Evaluate for Plasmodium parasites.
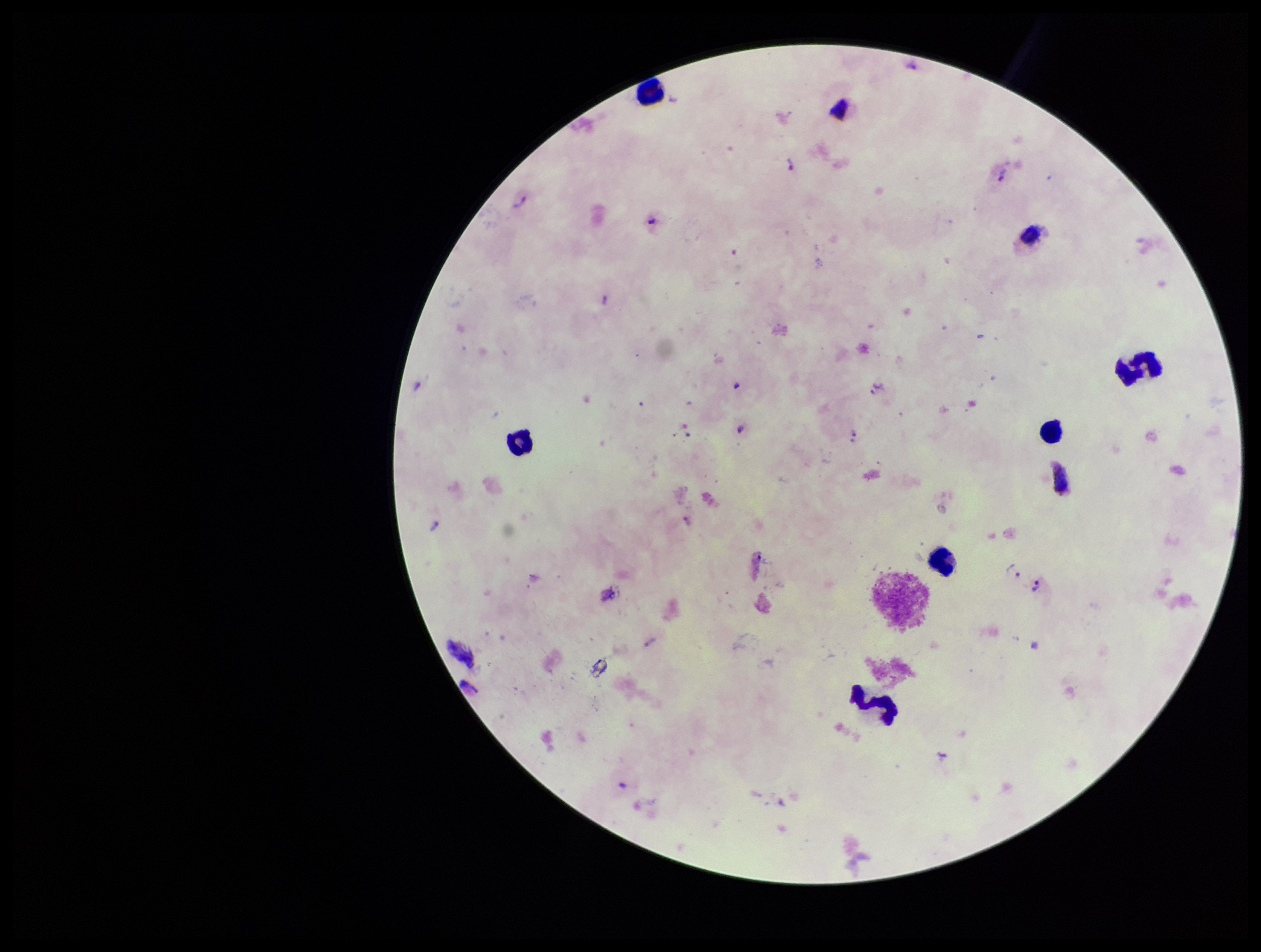
Identified.

stain = Giemsa
parasite count = 11
image size = 1261×952 pixels
patient malaria status = positive
preparation = thick smear
capture = smartphone photograph through the microscope eyepiece
species reported for this patient = Plasmodium vivax
field of view = single
leukocyte count = 8